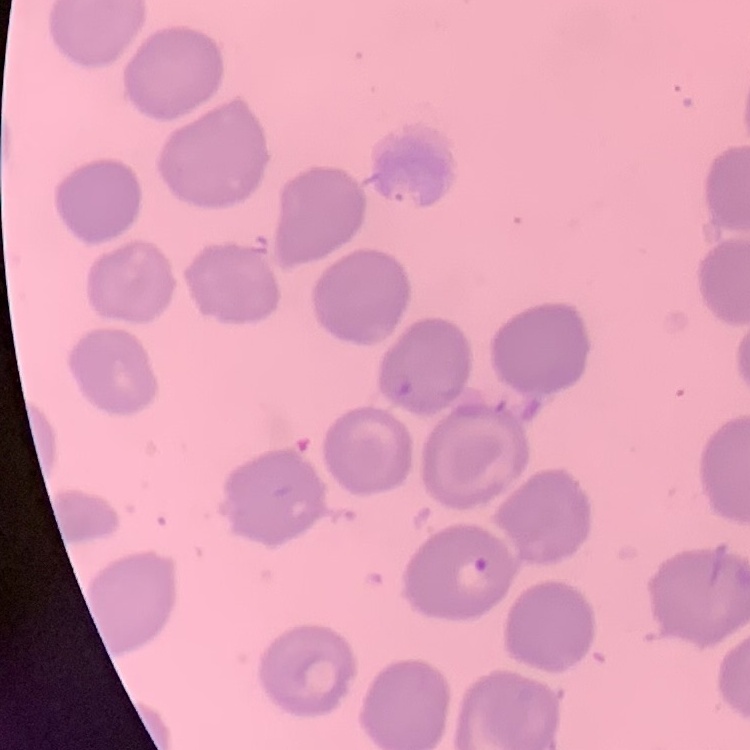

erythrocyte morphology = no rouleaux formation
stain = Field's or Giemsa
image type = square crop of a larger photomicrograph
preparation = thin peripheral smear